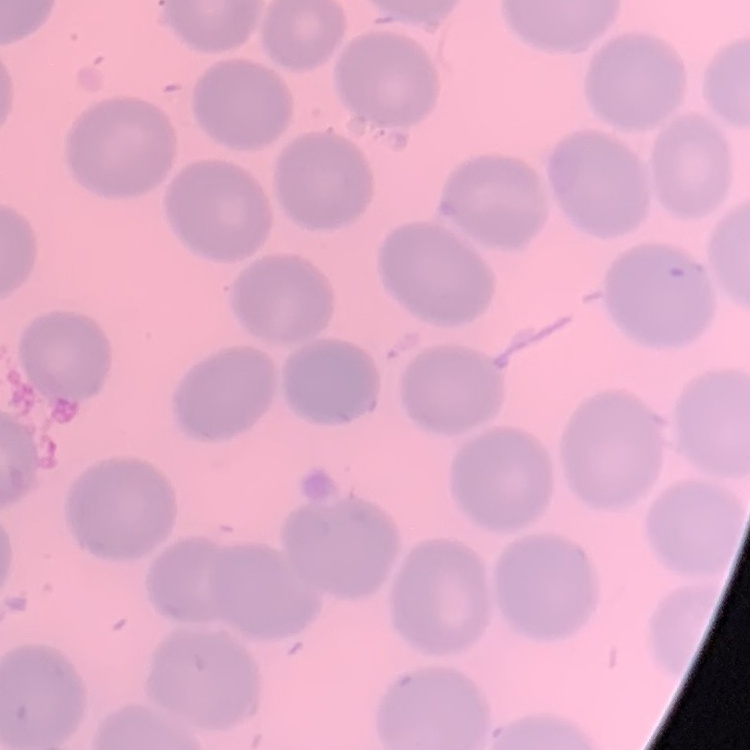

red_blood_cell_morphology: no rouleaux formation
image_type: one tile cut from a larger photomicrograph
stain: Field's or Giemsa
preparation: thin blood film